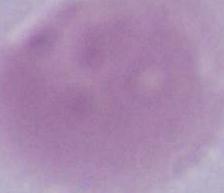

Summary:
  - Magnification: 1000x
  - Identification: erythrocyte
  - Modality: photomicrograph